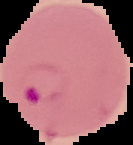
Result: malaria parasites identified. Cell region segmented out of the field of view; the surrounding area is masked to black. From a thin blood smear. Image is 133×145 pixels.